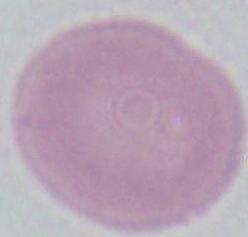
{
  "magnification": "1000x",
  "modality": "micrograph",
  "identification": "erythrocyte"
}